Assess this cell for malaria.
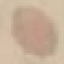

Uninfected.

Thin smear of blood. Automatically extracted cell patch, resized to 64 × 64 pixels. Giemsa-stained preparation. Acquired by smartphone through the microscope eyepiece.